Point out each leukocyte.
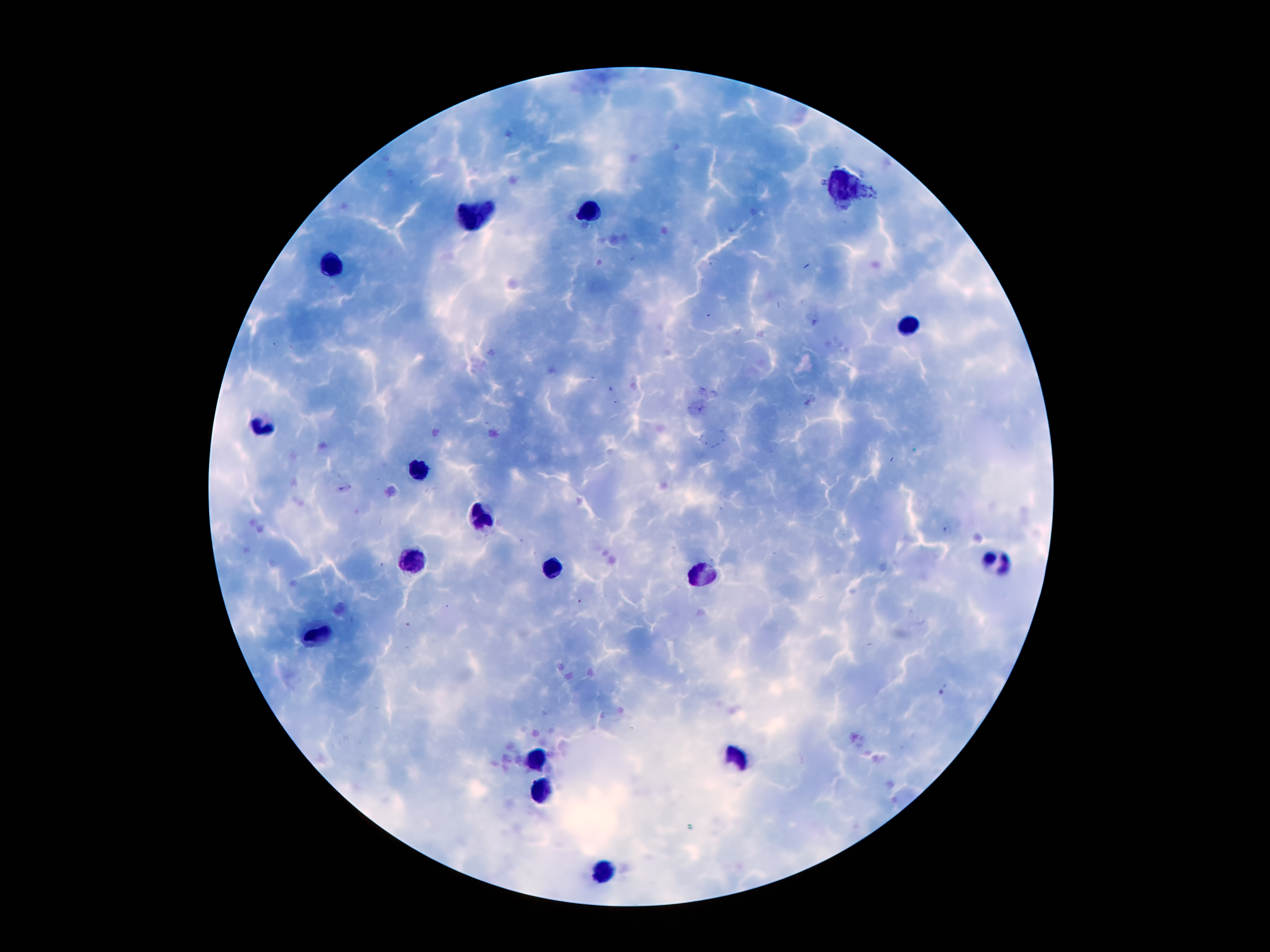

Approximate centers as {x, y} in pixels.
Leukocytes: {845, 184}, {593, 213}, {473, 216}, {334, 263}, {909, 325}, {262, 425}, {419, 468}, {485, 518}, {414, 561}, {993, 561}, {553, 568}, {704, 573}, {321, 634}, {737, 754}, {536, 757}, {543, 791}, {602, 870}.

Thick blood smear. Patient malaria status: infected with Plasmodium falciparum. Giemsa-stained preparation. One field from this slide. Image is 1270×952 pixels. Plasmodium parasites: not detected. Photographed through the microscope eyepiece with a smartphone camera. 100x magnification.